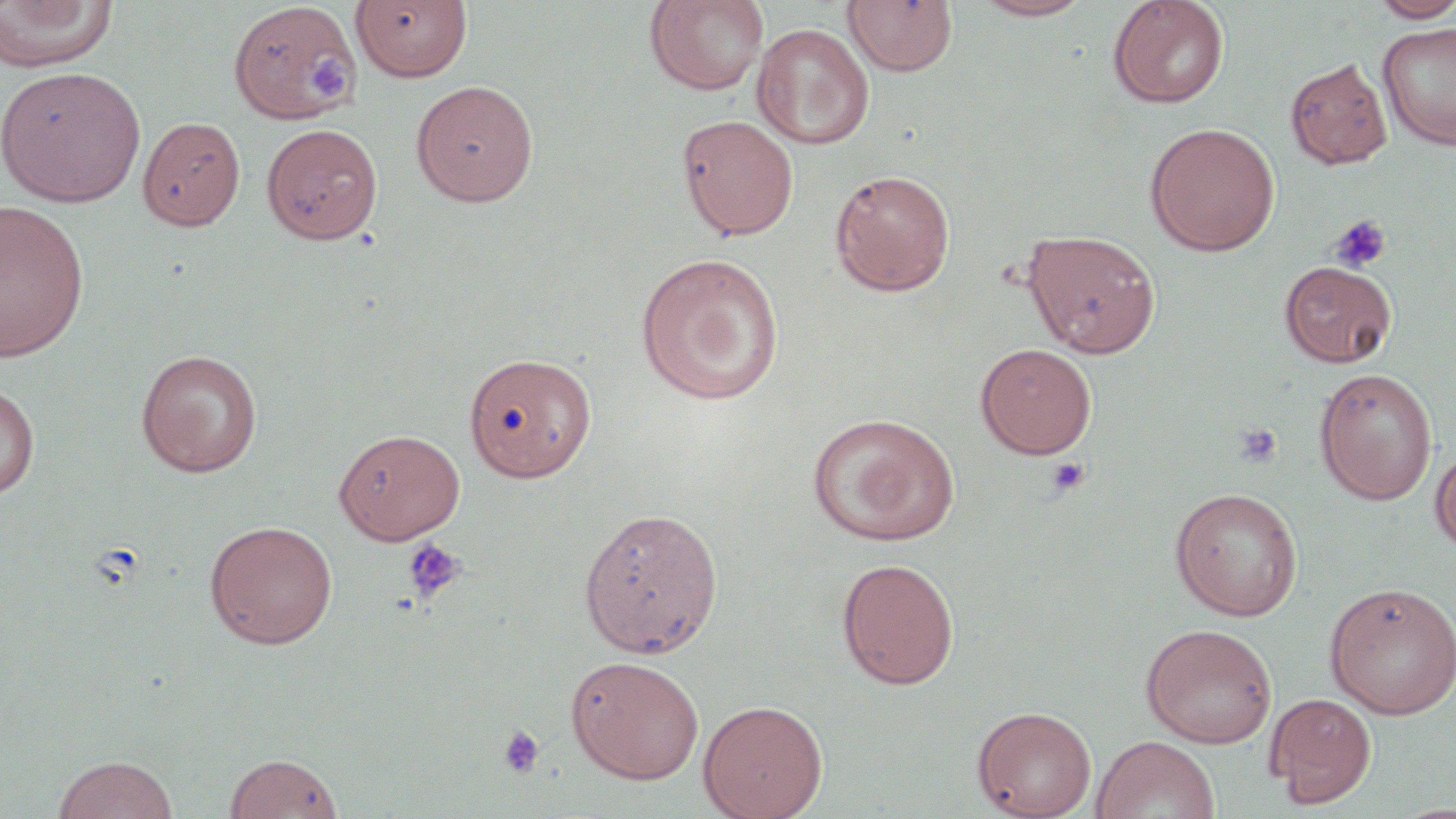

Summary:
  - Coordinate format: approximate bounding boxes as (x1, y1, x2, y2) in pixels
  - Platelet locations: (304, 53, 359, 109), (1328, 215, 1392, 273), (1234, 423, 1283, 468), (1046, 456, 1090, 496), (402, 538, 465, 604), (496, 724, 545, 780)
  - Uninfected red blood cell locations: (643, 0, 769, 96), (970, 0, 1098, 21), (1106, 0, 1230, 110), (1368, 0, 1456, 22), (0, 1, 119, 72), (350, 1, 473, 82), (842, 1, 958, 76), (228, 2, 362, 125), (1377, 20, 1456, 151), (752, 23, 875, 150), (1285, 58, 1393, 170), (0, 66, 146, 207), (410, 80, 539, 206), (677, 113, 799, 241), (137, 116, 246, 231), (1145, 122, 1281, 256), (261, 123, 384, 244), (829, 169, 956, 296), (0, 200, 91, 362), (1022, 228, 1161, 358), (634, 252, 786, 406), (1280, 261, 1396, 367), (975, 342, 1097, 459), (135, 349, 263, 476), (464, 351, 597, 482), (1314, 368, 1437, 505), (0, 382, 39, 501), (807, 412, 960, 546), (333, 428, 467, 544), (1430, 446, 1456, 558), (1169, 486, 1303, 621), (578, 505, 723, 658), (204, 520, 338, 649), (836, 557, 959, 689), (1323, 581, 1456, 719), (1140, 623, 1278, 748), (566, 655, 705, 784), (1264, 692, 1376, 807), (697, 699, 828, 819), (972, 705, 1097, 819), (1092, 735, 1220, 819), (223, 752, 344, 819), (52, 755, 178, 819)
  - Slide-level diagnosis: no evidence of blood parasites
  - Magnification: 1000x
  - Stain: May-Grünwald-Giemsa
  - Image size: 1456×819 pixels
  - Preparation: thin blood film
  - Modality: light microscopy
  - Field of view: one of a larger specimen